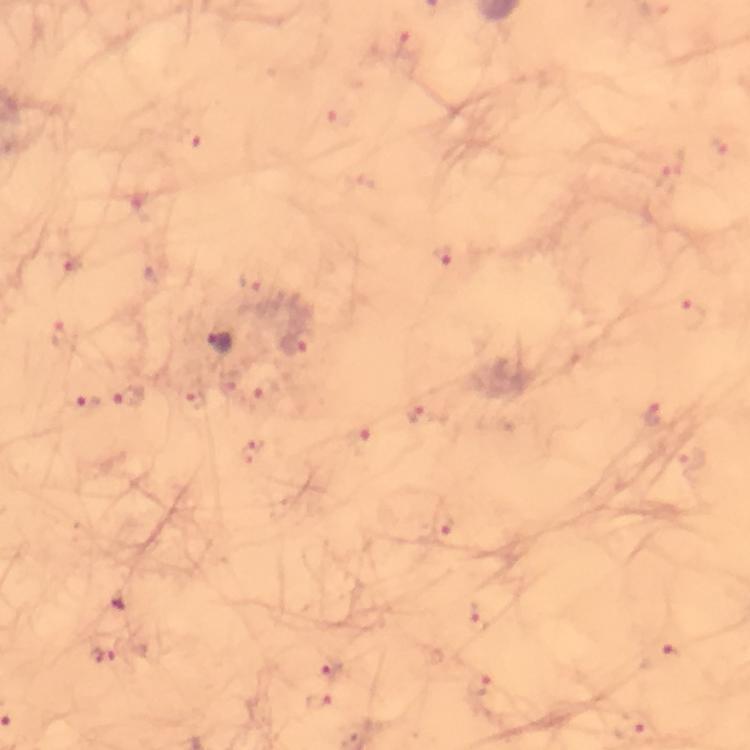
stain = Giemsa
immersion oil = used
magnification = 100x
capture = smartphone camera through the microscope
image size = 750×750 pixels
context = from a malaria diagnostic workup
preparation = thick smear
cropped from = one field of view
malaria parasite locations = approximate centers as (x, y) in pixels: (409, 45), (190, 140), (670, 181), (444, 253), (68, 263), (252, 278), (692, 314), (61, 335), (222, 343), (298, 344), (130, 397), (86, 404), (652, 412), (415, 413), (362, 440), (250, 451), (691, 460), (442, 526), (476, 618), (103, 655), (662, 657), (332, 666), (481, 684), (317, 701)